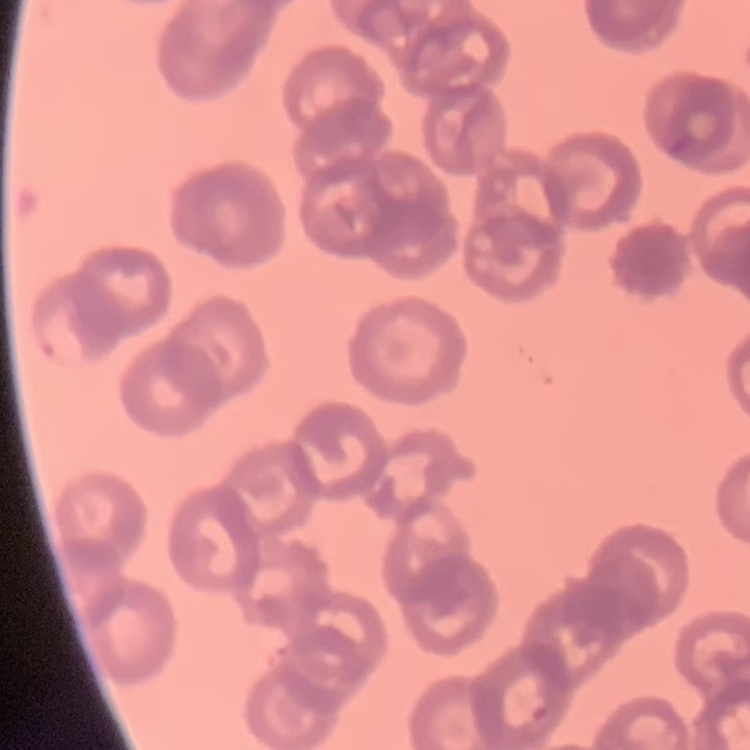

red_blood_cell_morphology: rouleaux formation
preparation: thin peripheral smear
stain: Field's or Giemsa
image_type: one tile cut from a larger photomicrograph